Comment on the morphology of the red blood cells.
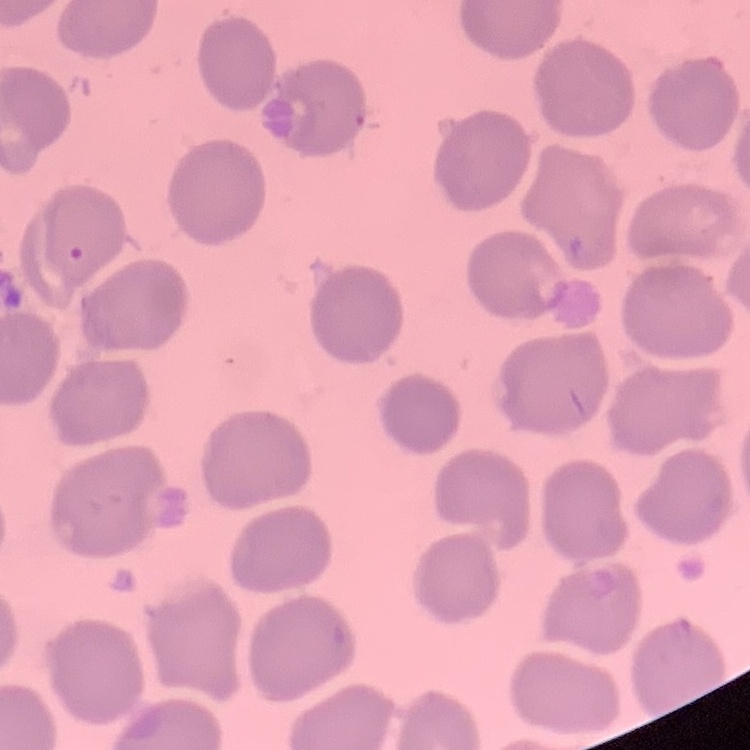
No rouleaux formation.

stain: Field's or Giemsa
preparation: thin peripheral smear
image_type: one tile cut from a larger photomicrograph